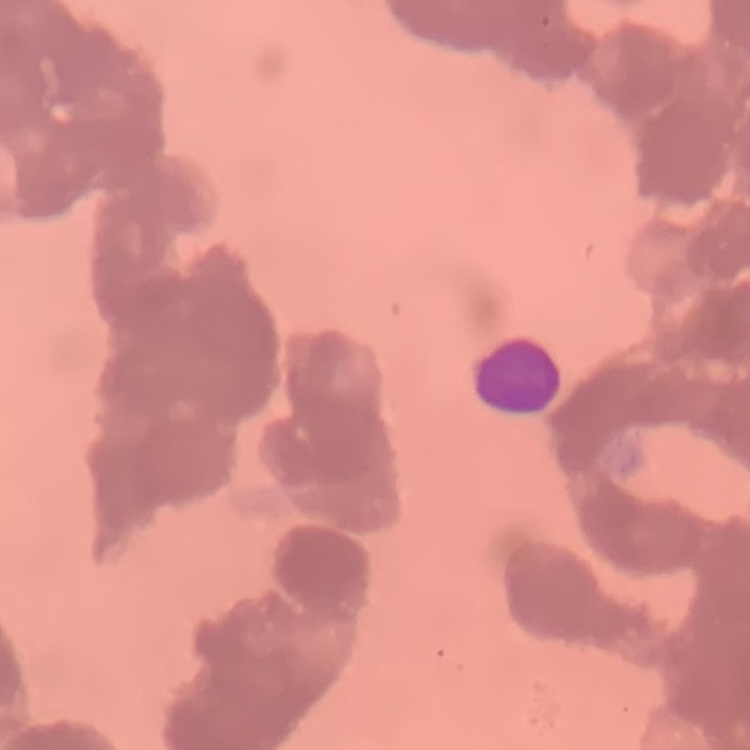

The erythrocytes show rouleaux formation. One tile cut from a larger photomicrograph. Field's or Giemsa stain. Thin blood smear.